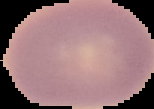 The area outside the segmented cell region is set to black. From a thin blood smear. Image is 154×109 pixels. Result: no Plasmodium parasites detected.